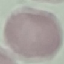
result = no malaria parasites detected
image type = cell patch, automatically extracted from a larger field of view and resized to 64 × 64 pixels
capture = smartphone through the microscope eyepiece
stain = Giemsa
preparation = thin smear